Locate every Plasmodium parasite.
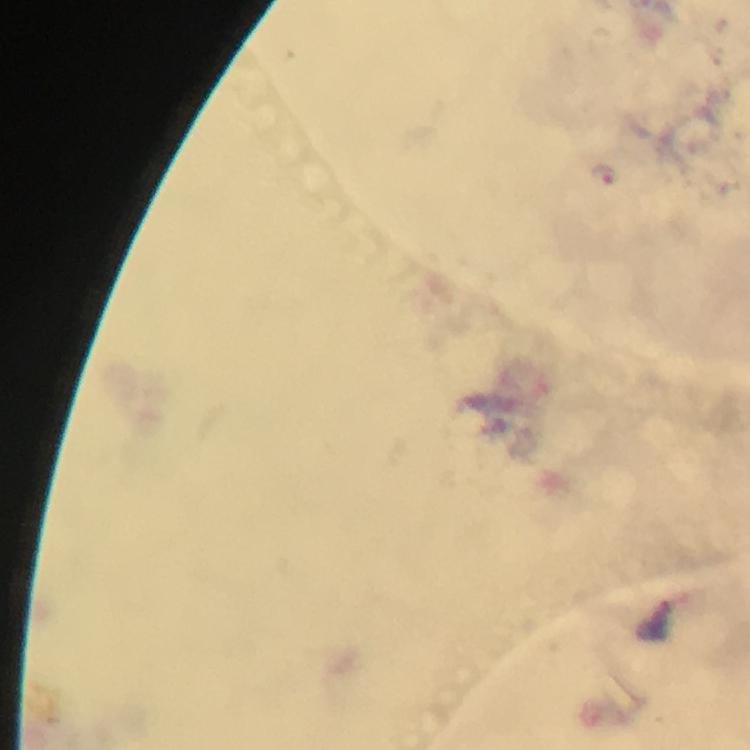
Approximate centers as (x, y) in pixels.
Plasmodium parasites: (605, 176).

Thick blood smear. Giemsa stain. Immersion oil was used. From a malaria diagnostic workup. Cropped region of a single field of view. Smartphone photograph taken through a microscope. Image is 750×750 pixels. 100x magnification.